Classify this cell by malaria status.
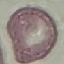

It is uninfected.

image type = automatically extracted cell patch, resized to 64 × 64 pixels
stain = Giemsa
capture = smartphone through the microscope eyepiece
preparation = thin blood film